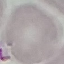
Result: no malaria parasites seen. Giemsa-stained preparation. Cell patch, automatically extracted from a larger field of view and resized to 64 × 64 pixels. Photographed with a smartphone camera at the microscope eyepiece. Thin blood smear.